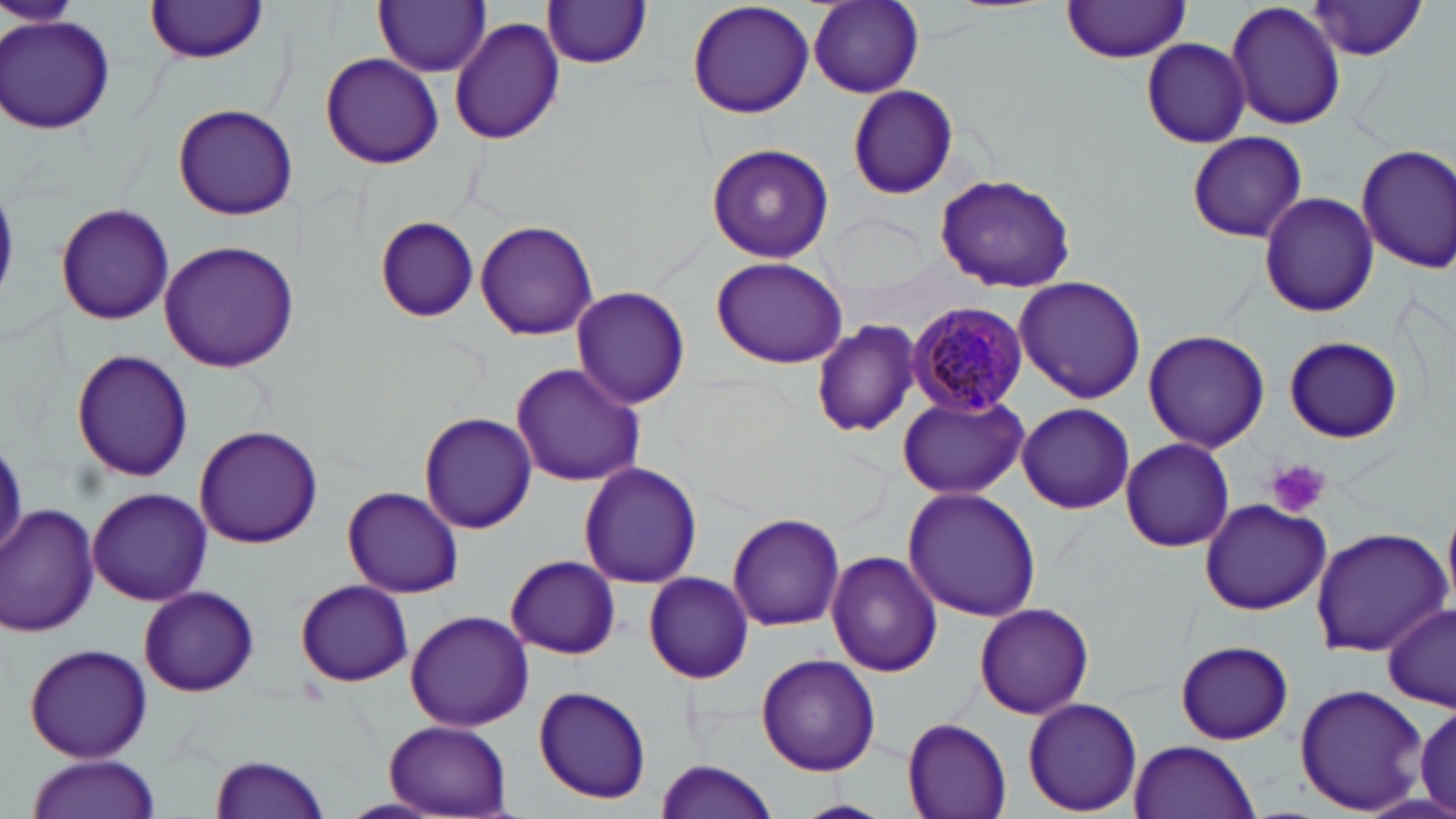
{
  "slide_level_diagnosis": "Plasmodium malariae",
  "modality": "optical microscopy",
  "preparation": "thin blood smear",
  "image_size": "1456×819 pixels",
  "plasmodium_malariae_infected_red_blood_cell_locations": "approximate bounding boxes as (x1,y1)-(x2,y2) corner pairs in pixels: (906,300)-(1029,418)",
  "platelet_locations": "approximate bounding boxes as (x1,y1)-(x2,y2) corner pairs in pixels: (1267,460)-(1329,519)",
  "magnification": "1000x",
  "field_of_view": "single",
  "stain": "May-Grünwald-Giemsa",
  "uninfected_red_blood_cell_locations": "approximate bounding boxes as (x1,y1)-(x2,y2) corner pairs in pixels: (0,0)-(77,32), (145,0)-(269,63), (373,0)-(489,77), (687,0)-(815,120), (808,0)-(924,97), (1060,1)-(1195,63), (1225,1)-(1347,132), (1306,1)-(1429,59), (541,2)-(654,68), (2,12)-(116,135), (448,18)-(565,144), (1139,39)-(1251,146), (320,53)-(444,170), (847,86)-(959,199), (172,103)-(299,220), (1186,131)-(1308,243), (705,142)-(834,264), (1356,142)-(1456,274), (934,173)-(1079,293), (1259,193)-(1379,318), (56,202)-(176,325), (829,213)-(929,293), (375,217)-(479,321), (475,218)-(600,341), (158,241)-(299,373), (710,256)-(847,369), (1015,276)-(1147,403), (570,287)-(690,406), (810,320)-(920,437), (1142,329)-(1271,452), (1285,334)-(1402,444), (72,350)-(193,483), (510,359)-(647,488), (898,394)-(1028,499), (1016,401)-(1137,512), (419,413)-(538,535), (193,425)-(323,549), (1118,436)-(1236,554), (0,442)-(29,551), (577,462)-(702,590), (343,486)-(464,599), (88,488)-(213,605), (902,488)-(1041,621), (1199,498)-(1331,614), (1,504)-(100,637), (727,512)-(845,632), (1309,527)-(1451,655), (825,552)-(941,678), (505,554)-(621,659), (643,570)-(755,683), (296,579)-(412,687), (138,585)-(258,694), (973,601)-(1095,718), (1381,604)-(1455,710), (404,609)-(535,731), (1175,640)-(1294,744), (23,642)-(153,762), (757,653)-(880,775), (1293,682)-(1432,815), (531,684)-(654,805), (1023,697)-(1143,815), (1411,702)-(1456,814), (901,717)-(1013,819), (382,718)-(513,816), (1129,739)-(1260,819), (210,753)-(333,818), (24,756)-(160,819), (653,758)-(780,819), (792,798)-(892,819)"
}